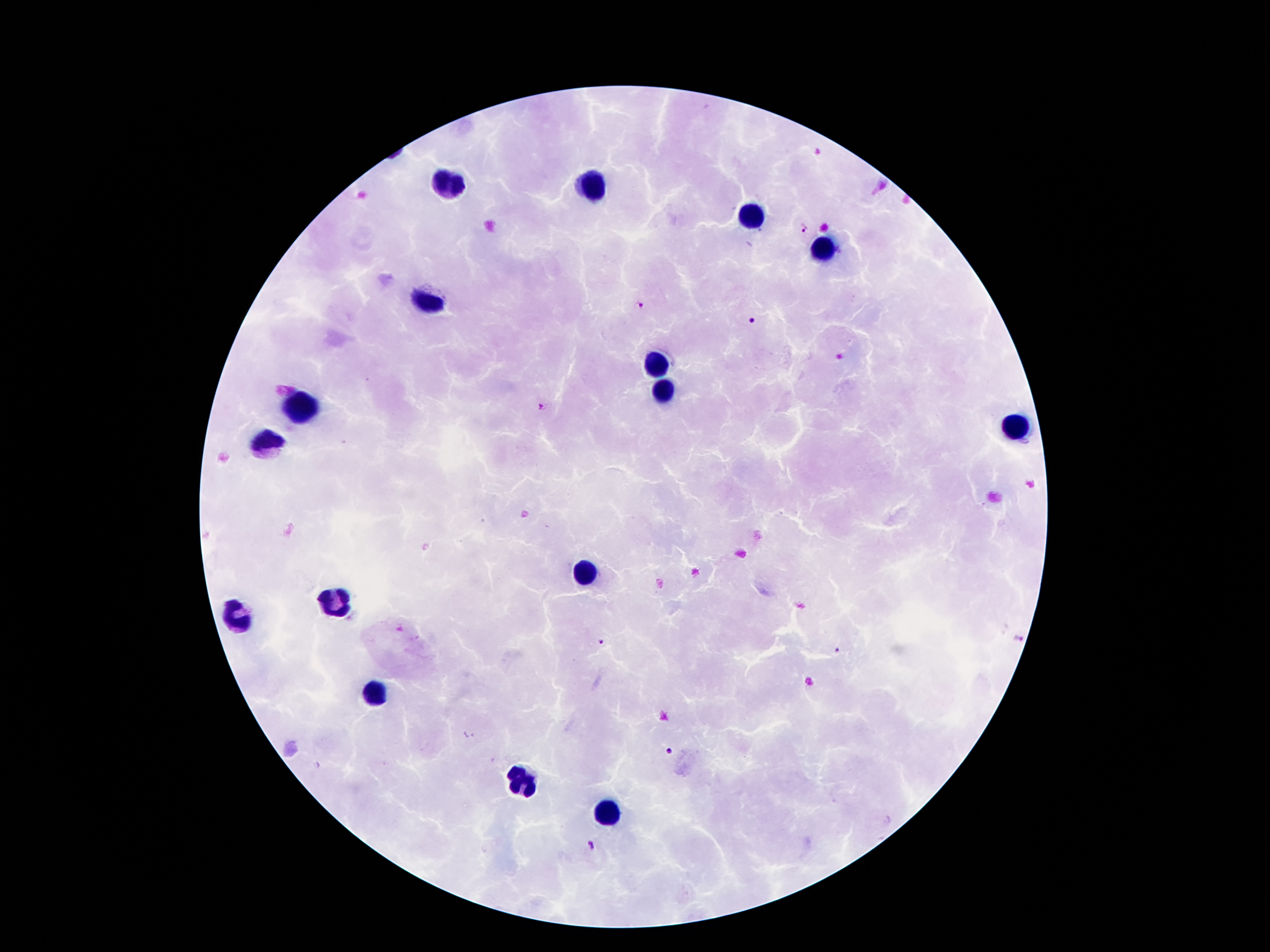

coordinate format = approximate centers as (x, y) in pixels
leukocyte locations = (451, 187), (593, 187), (753, 218), (824, 252), (426, 300), (658, 365), (660, 387), (300, 410), (1017, 428), (272, 441), (585, 567), (333, 605), (237, 618), (373, 697), (518, 777), (602, 811)
Plasmodium parasite locations = (802, 228), (640, 306), (752, 321), (542, 406), (1017, 639), (602, 641), (837, 652), (668, 751), (591, 845)
preparation = thick blood smear
capture = smartphone camera through the microscope eyepiece
patient malaria status = infected with Plasmodium falciparum
magnification = 100x
stain = Giemsa
image size = 1270×952 pixels
field of view = single